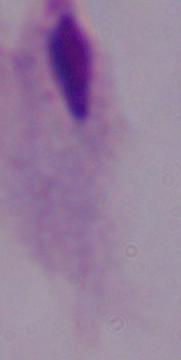
A trichomonad is seen. Micrograph. Captured at 1000x magnification.